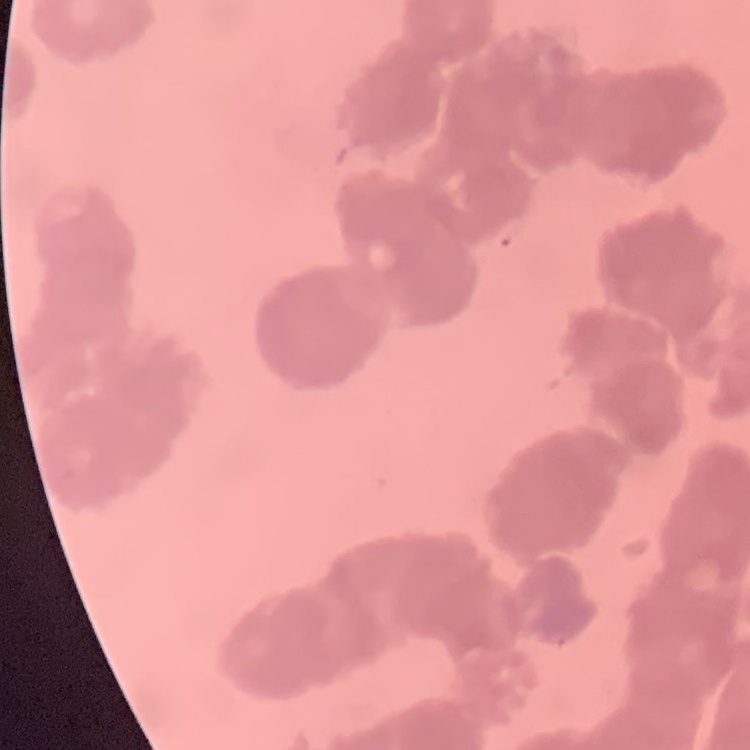
The red blood cells exhibit rouleaux formation. Stained with either Field's or Giemsa. Square crop of a larger photomicrograph. Thin blood film.